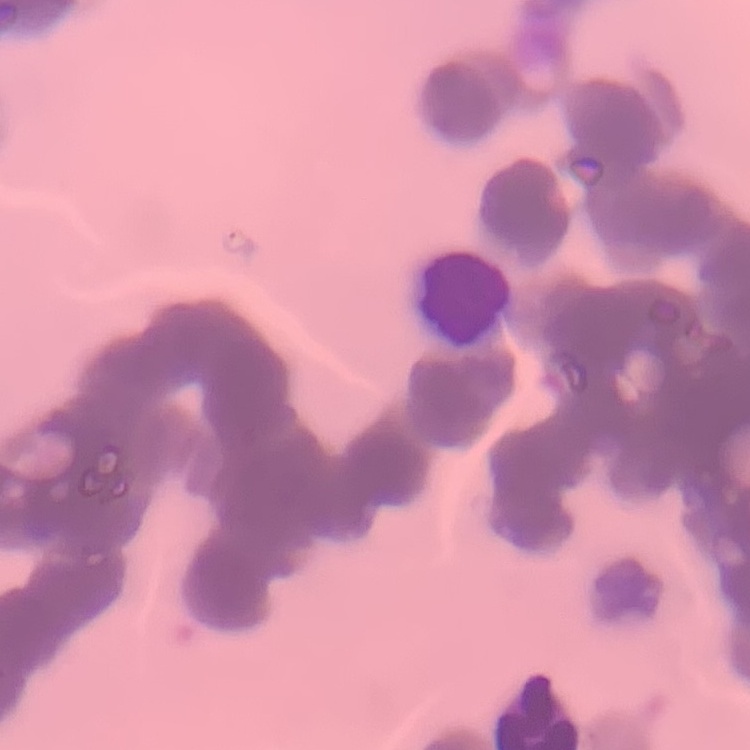

{
  "red_blood_cell_morphology": "rouleaux formation",
  "preparation": "thin peripheral smear",
  "image_type": "one tile cut from a larger photomicrograph",
  "stain": "Field's or Giemsa"
}